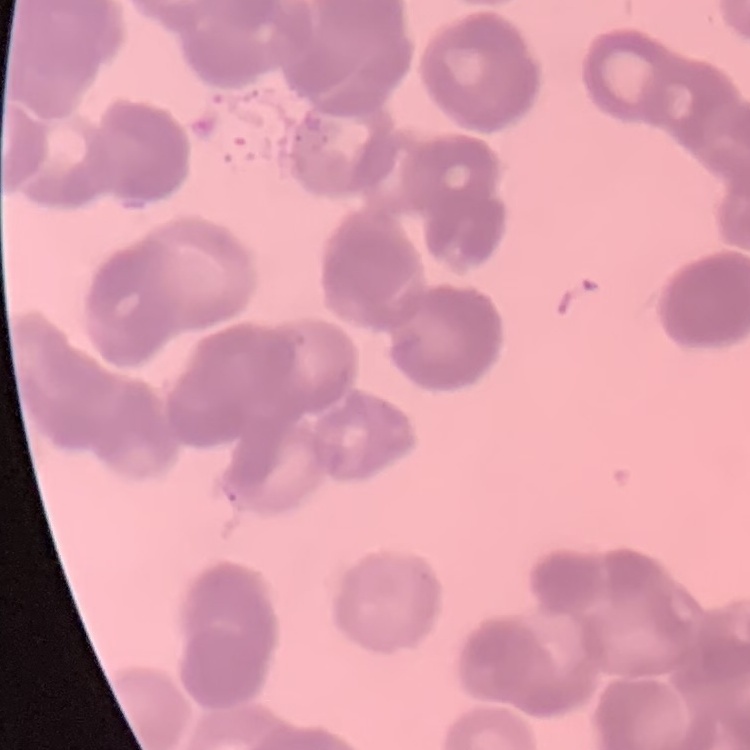
erythrocyte_morphology: rouleaux formation
stain: Field's or Giemsa
image_type: one tile cut from a larger photomicrograph
preparation: thin blood smear